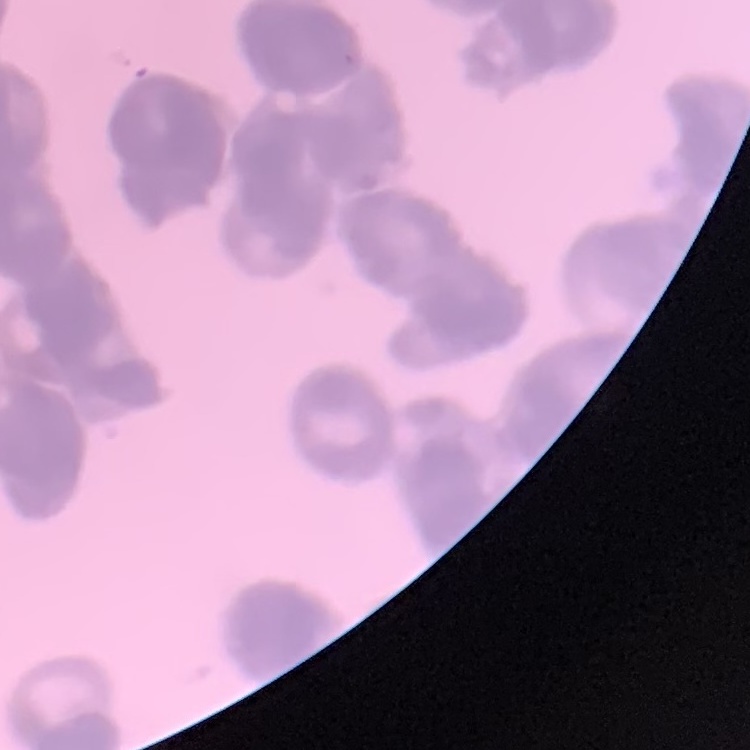

The red blood cells exhibit rouleaux formation. Field's or Giemsa stain. Square crop of a larger photomicrograph. Thin peripheral smear.